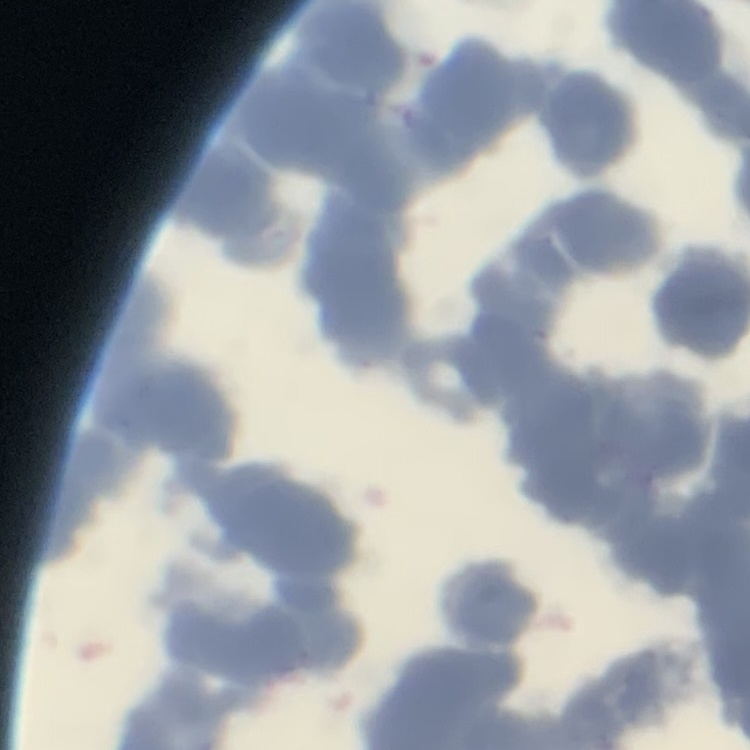

erythrocyte morphology = rouleaux formation
preparation = thin blood film
stain = Field's or Giemsa
image type = square crop of a larger photomicrograph